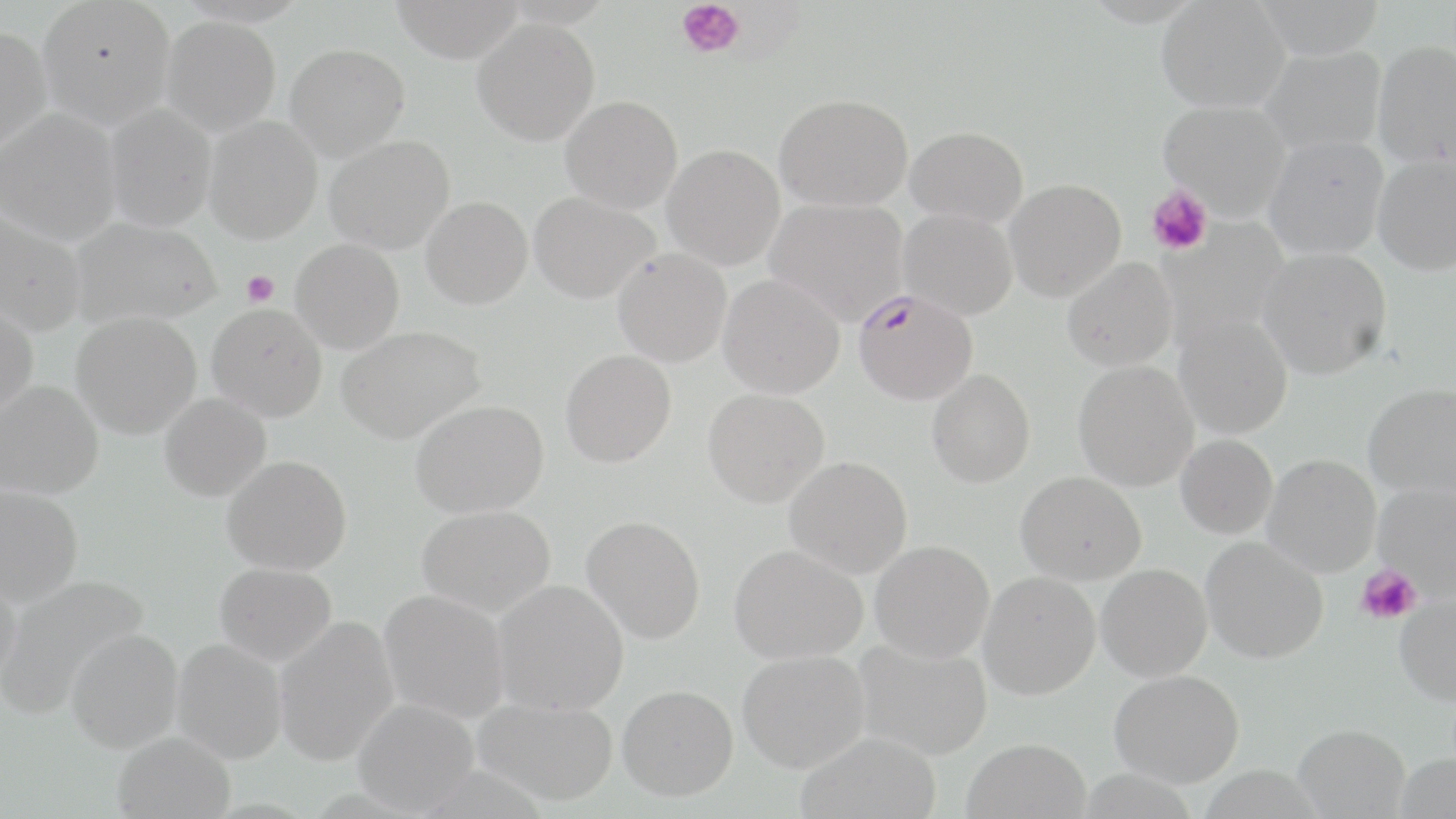

slide-level diagnosis = Plasmodium falciparum
uninfected red blood cell locations = approximate bounding boxes as [x1, y1, x2, y2] in pixels: [37, 0, 176, 129], [390, 0, 524, 63], [1252, 0, 1387, 61], [1156, 1, 1290, 113], [161, 16, 281, 136], [472, 19, 600, 145], [0, 27, 52, 156], [1372, 40, 1456, 169], [285, 44, 410, 161], [1259, 46, 1386, 156], [775, 93, 914, 211], [560, 96, 683, 213], [1158, 100, 1291, 219], [103, 104, 216, 232], [0, 108, 121, 245], [204, 116, 323, 244], [906, 126, 1029, 227], [1263, 135, 1389, 260], [325, 136, 455, 254], [663, 144, 785, 270], [1372, 154, 1456, 276], [1003, 179, 1126, 302], [529, 191, 660, 303], [421, 196, 532, 309], [765, 198, 909, 323], [0, 207, 88, 336], [899, 209, 1018, 320], [70, 217, 221, 328], [290, 239, 405, 354], [1257, 247, 1392, 379], [612, 248, 732, 367], [1062, 258, 1178, 371], [718, 274, 845, 399], [0, 301, 38, 423], [206, 303, 327, 422], [71, 312, 202, 439], [1174, 315, 1293, 439], [336, 325, 486, 444], [561, 349, 677, 467], [1073, 360, 1198, 491], [927, 369, 1035, 488], [0, 380, 104, 499], [1363, 382, 1456, 501], [703, 388, 829, 507], [158, 392, 271, 501], [410, 399, 549, 518], [1176, 434, 1278, 539], [1263, 454, 1382, 577], [222, 455, 352, 575], [785, 456, 913, 579], [1016, 471, 1146, 585], [1373, 483, 1456, 599], [0, 484, 84, 607], [417, 504, 556, 617], [582, 515, 706, 643], [1200, 536, 1329, 664], [869, 540, 995, 663], [729, 543, 868, 664], [215, 562, 337, 666], [1096, 563, 1213, 681], [0, 567, 22, 690], [978, 572, 1101, 700], [0, 573, 149, 720], [492, 579, 629, 716], [378, 589, 509, 723], [1394, 593, 1456, 705], [273, 616, 399, 766], [65, 627, 184, 753], [173, 639, 288, 763], [852, 639, 993, 761], [737, 649, 870, 773], [1109, 669, 1244, 787], [617, 684, 738, 800], [473, 697, 618, 806], [351, 699, 479, 816], [1292, 723, 1410, 818], [112, 731, 235, 818], [796, 731, 941, 819], [961, 738, 1091, 819]
image size = 1456×819 pixels
stain = May-Grünwald-Giemsa
platelet locations = approximate bounding boxes as [x1, y1, x2, y2] in pixels: [675, 0, 745, 59], [1146, 185, 1213, 255], [242, 271, 279, 306], [1357, 567, 1421, 625]
modality = light microscopy
magnification = 1000x
preparation = thin blood smear
Plasmodium falciparum-infected red blood cell locations = approximate bounding boxes as [x1, y1, x2, y2] in pixels: [851, 287, 979, 405]
field of view = one of a larger specimen